Locate every malaria parasite.
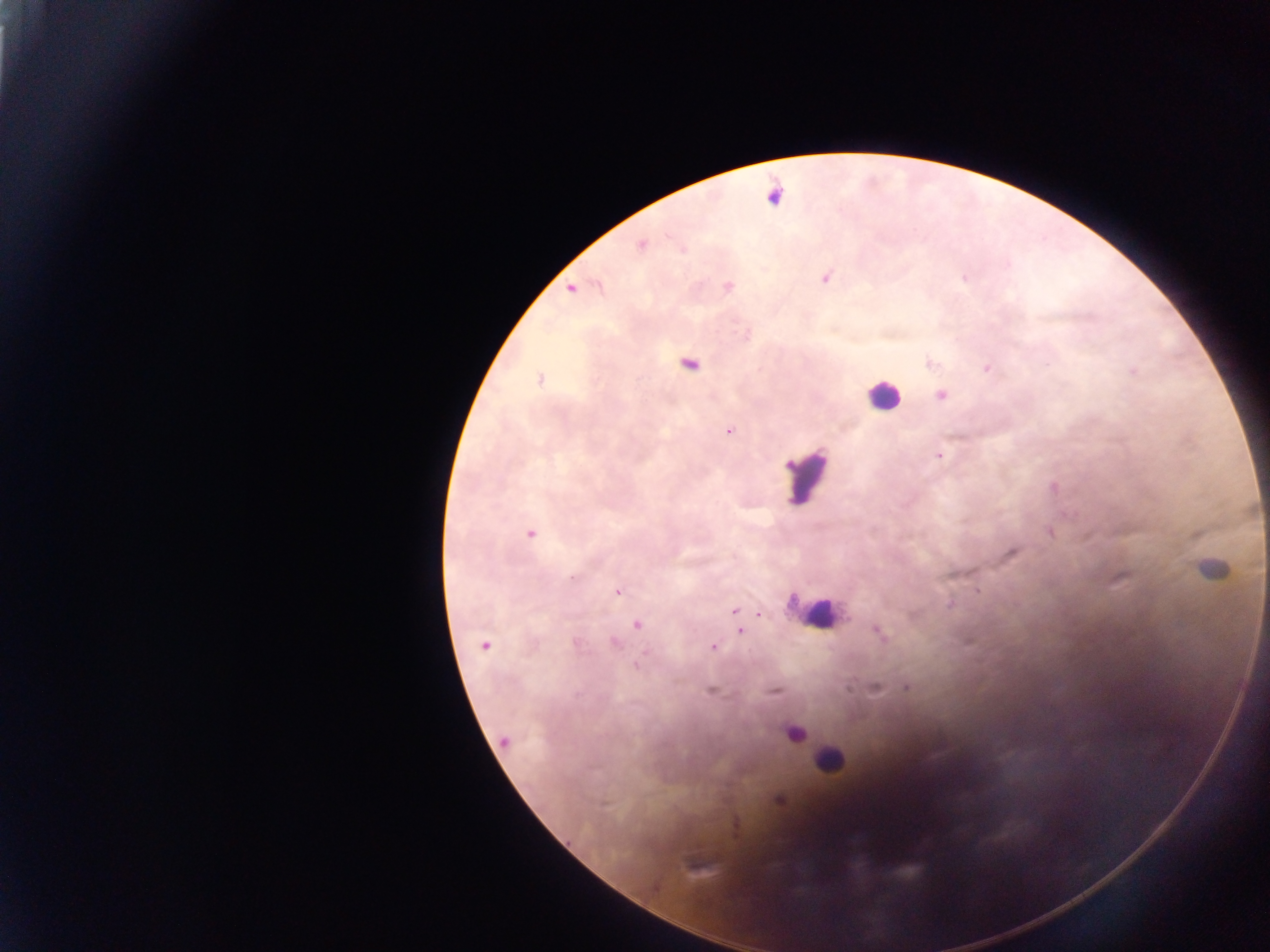
Approximate centers as x y in pixels.
Malaria parasites: 641 245; 826 279; 728 287; 571 289; 690 365; 987 368; 1133 371; 540 379; 941 396; 729 430; 939 455; 1051 532; 530 533; 1013 552; 572 578; 1119 578; 978 591; 617 592; 950 604; 734 612; 638 624; 740 632; 878 632; 614 643; 485 645; 713 647; 638 665; 906 687; 875 689; 711 691; 774 692; 505 740; 778 800.

Leukocyte locations: 882 395; 805 476; 1211 569; 815 615; 794 732; 830 759. Thick blood film. Single field of view. Image is 1270×952 pixels. Photographed through a microscope with a mobile-phone camera. Collected in Ghana.